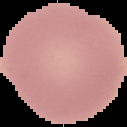
Summary:
  - Preparation: thin blood smear
  - Result: no Plasmodium parasites detected
  - Image size: 127×127 pixels
  - Image type: segmented cell region with the area outside set to black